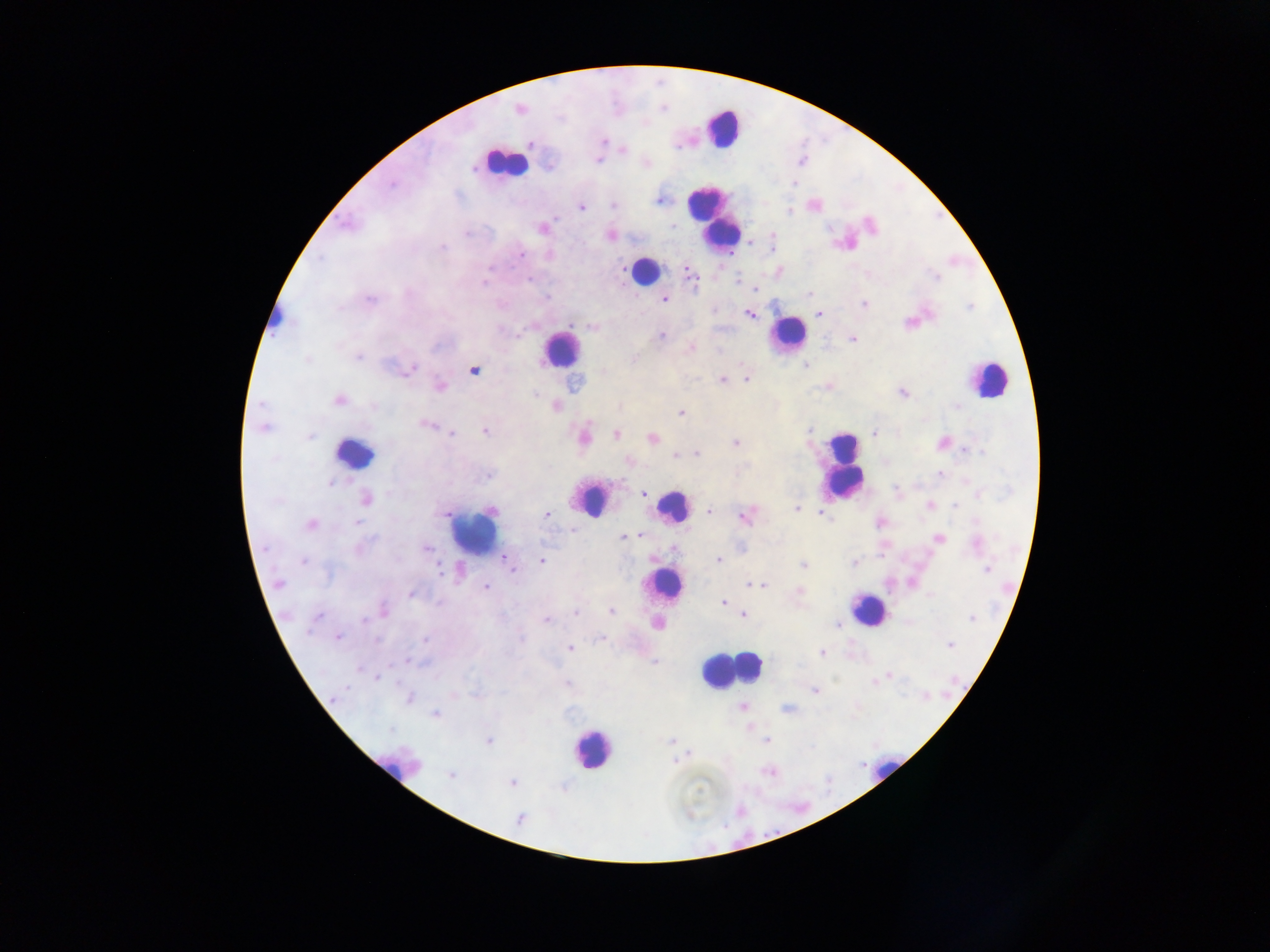

Approximate centers as (x, y) in pixels. Leukocyte locations: (721, 127), (506, 163), (713, 217), (644, 271), (278, 316), (788, 333), (560, 349), (987, 379), (354, 452), (843, 465), (591, 498), (673, 505), (474, 533), (667, 583), (868, 608), (730, 670), (590, 749), (396, 762), (881, 771). Malaria parasite locations: (519, 109), (604, 142), (531, 144), (597, 160), (474, 169), (794, 183), (391, 184), (659, 201), (614, 206), (582, 208), (789, 211), (345, 222), (542, 229), (467, 234), (609, 236), (443, 246), (521, 255), (319, 258), (489, 268), (690, 274), (936, 278), (530, 280), (484, 283), (809, 294), (370, 300), (664, 300), (864, 304), (339, 308), (819, 314), (750, 315), (571, 324), (592, 327), (518, 335), (661, 336), (853, 339), (358, 357), (307, 359), (741, 364), (806, 366), (412, 370), (474, 371), (746, 379), (721, 380), (575, 384), (440, 387), (902, 393), (535, 394), (339, 400), (261, 403), (373, 406), (557, 406), (956, 406), (681, 413), (426, 425), (263, 428), (809, 430), (484, 431), (874, 433), (451, 434), (617, 435), (309, 436), (583, 437), (653, 437), (735, 443), (941, 443), (966, 450), (981, 451), (697, 454), (677, 455), (629, 461), (940, 474), (489, 477), (330, 483), (643, 493), (978, 494), (367, 498), (930, 506), (954, 506), (796, 508), (710, 511), (546, 514), (823, 515), (745, 517), (359, 522), (310, 524), (573, 528), (636, 536), (623, 537), (939, 538), (976, 543), (427, 548), (265, 549), (359, 549), (505, 559), (719, 559), (542, 561), (303, 562), (509, 563), (855, 563), (803, 565), (512, 568), (440, 570), (986, 570), (329, 575), (278, 584), (750, 585), (761, 586), (486, 587), (800, 590), (411, 594), (931, 596), (723, 603), (384, 609), (611, 611), (575, 612), (743, 615), (317, 617), (972, 618), (364, 620), (546, 620), (837, 625), (338, 637), (601, 638), (425, 639), (377, 641), (950, 644), (570, 648), (822, 653), (409, 662), (655, 662), (359, 668), (890, 676), (378, 677), (567, 682), (874, 682), (345, 688), (814, 691), (926, 696), (409, 698), (742, 707), (787, 709), (435, 714), (390, 730), (766, 740), (489, 741), (670, 742), (683, 757), (676, 761), (768, 772), (451, 776), (512, 783), (520, 818). Thick blood film. Collected in Ghana. Image is 1270×952 pixels. Photographed through a microscope with a mobile-phone camera. One field of view.